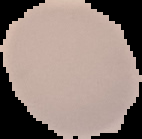 From a thin blood film. Result: negative for Plasmodium parasites. Image is 142×139 pixels. The area outside the segmented cell region is set to black.